Report the malaria status of this cell.
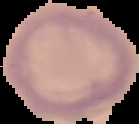

It is uninfected.

preparation: thin blood smear
image_type: segmented cell region with the area outside set to black
image_size: 139×124 pixels